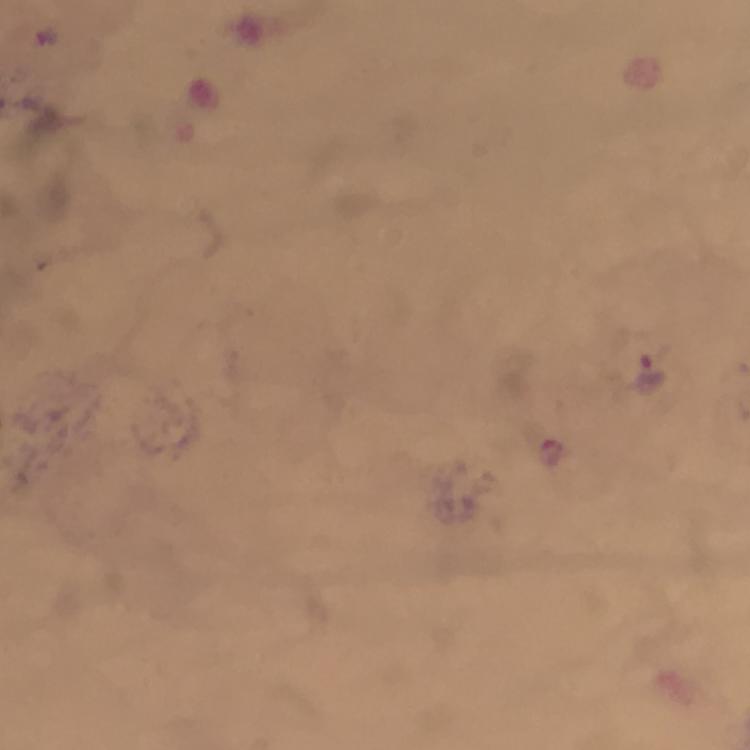
immersion oil = used
stain = Giemsa
cropped from = a single field of view
context = from a malaria diagnostic workup
preparation = thick blood film
capture = smartphone mounted on the microscope
image size = 750×750 pixels
Plasmodium parasite locations = approximate centers as [x, y] in pixels: [651, 372], [550, 452]
magnification = 100x